Identify the blood parasite species.
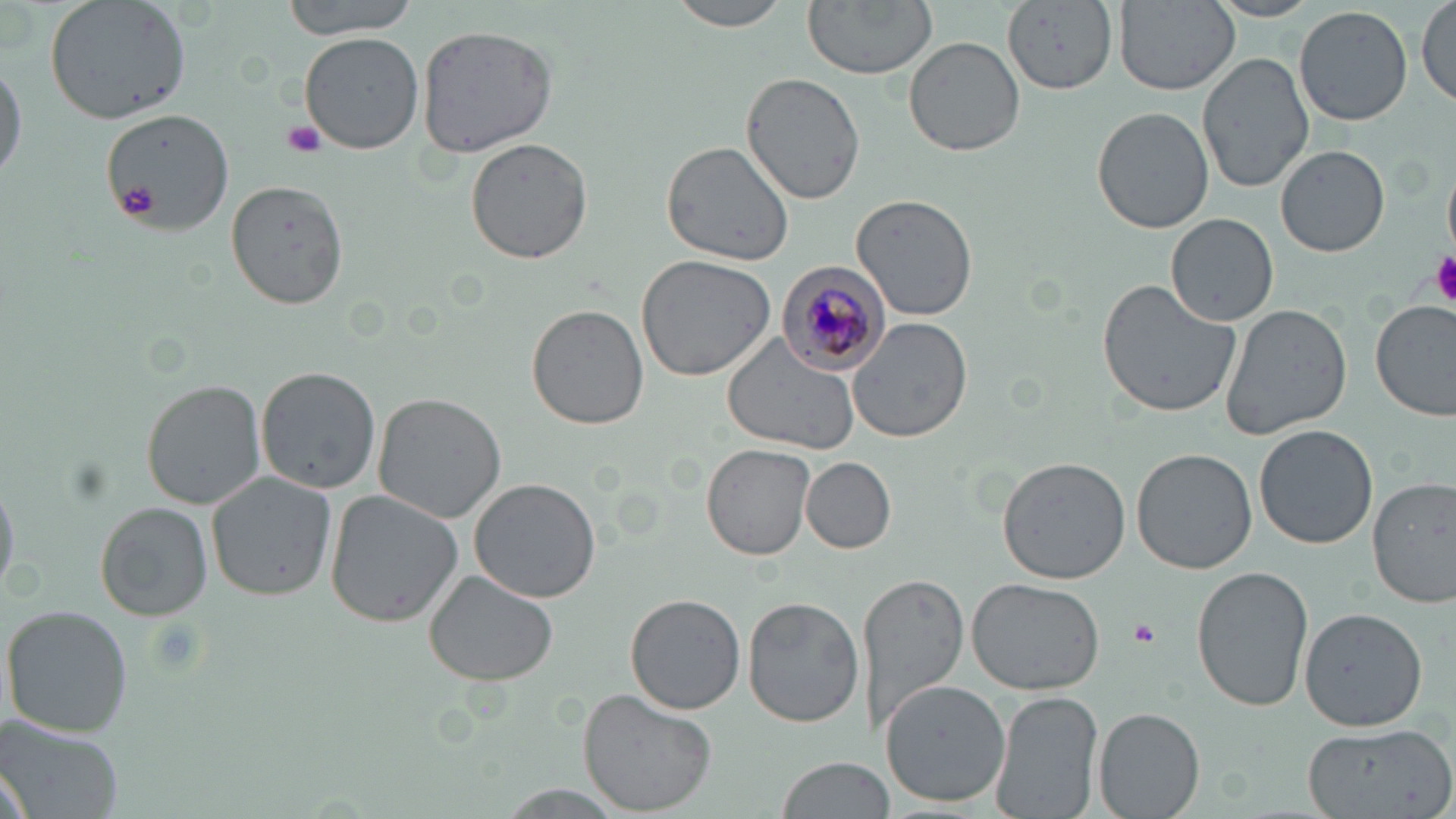

Plasmodium malariae.

Approximate bounding boxes as [x1, y1, x2, y2] in pixels. Plasmodium malariae-infected red blood cell locations: [778, 261, 895, 373]. Platelet locations: [280, 120, 330, 159], [119, 188, 158, 219], [1429, 250, 1456, 302], [1126, 617, 1161, 649]. Uninfected red blood cell locations: [44, 0, 192, 124], [285, 0, 418, 39], [665, 0, 796, 32], [802, 0, 938, 79], [1114, 0, 1238, 94], [1205, 0, 1324, 22], [1415, 0, 1455, 109], [1000, 1, 1119, 96], [1295, 6, 1413, 127], [416, 23, 557, 158], [298, 31, 424, 154], [905, 36, 1025, 156], [1198, 53, 1315, 193], [0, 59, 25, 188], [740, 72, 866, 205], [1094, 106, 1215, 233], [102, 107, 234, 235], [465, 138, 594, 265], [659, 140, 796, 267], [1277, 145, 1390, 256], [221, 176, 349, 311], [851, 194, 979, 321], [1167, 214, 1278, 325], [635, 254, 775, 382], [1097, 277, 1244, 419], [1371, 300, 1455, 422], [527, 304, 648, 430], [1218, 304, 1352, 439], [846, 317, 973, 444], [721, 333, 863, 455], [255, 363, 381, 495], [142, 380, 267, 508], [372, 392, 507, 523], [1255, 425, 1377, 549], [701, 444, 815, 560], [1281, 444, 1420, 583], [1132, 448, 1257, 573], [997, 456, 1131, 583], [801, 457, 896, 553], [207, 472, 336, 600], [0, 473, 17, 601], [1368, 476, 1455, 607], [470, 479, 603, 605], [324, 490, 462, 628], [96, 503, 211, 620], [1191, 566, 1314, 711], [859, 569, 970, 739], [424, 571, 559, 685], [965, 576, 1105, 695], [624, 593, 746, 714], [742, 597, 864, 729], [3, 605, 133, 736], [1298, 605, 1429, 732], [880, 679, 1010, 808], [577, 686, 718, 814], [991, 689, 1103, 819], [1094, 707, 1205, 819], [0, 717, 125, 819], [1299, 720, 1454, 819], [775, 755, 892, 819], [1, 758, 34, 819], [491, 784, 630, 815]. 1000x magnification. Image is 1456×819 pixels. May-Grünwald-Giemsa stain. Optical microscopy. One field of a larger specimen. Thin blood smear.